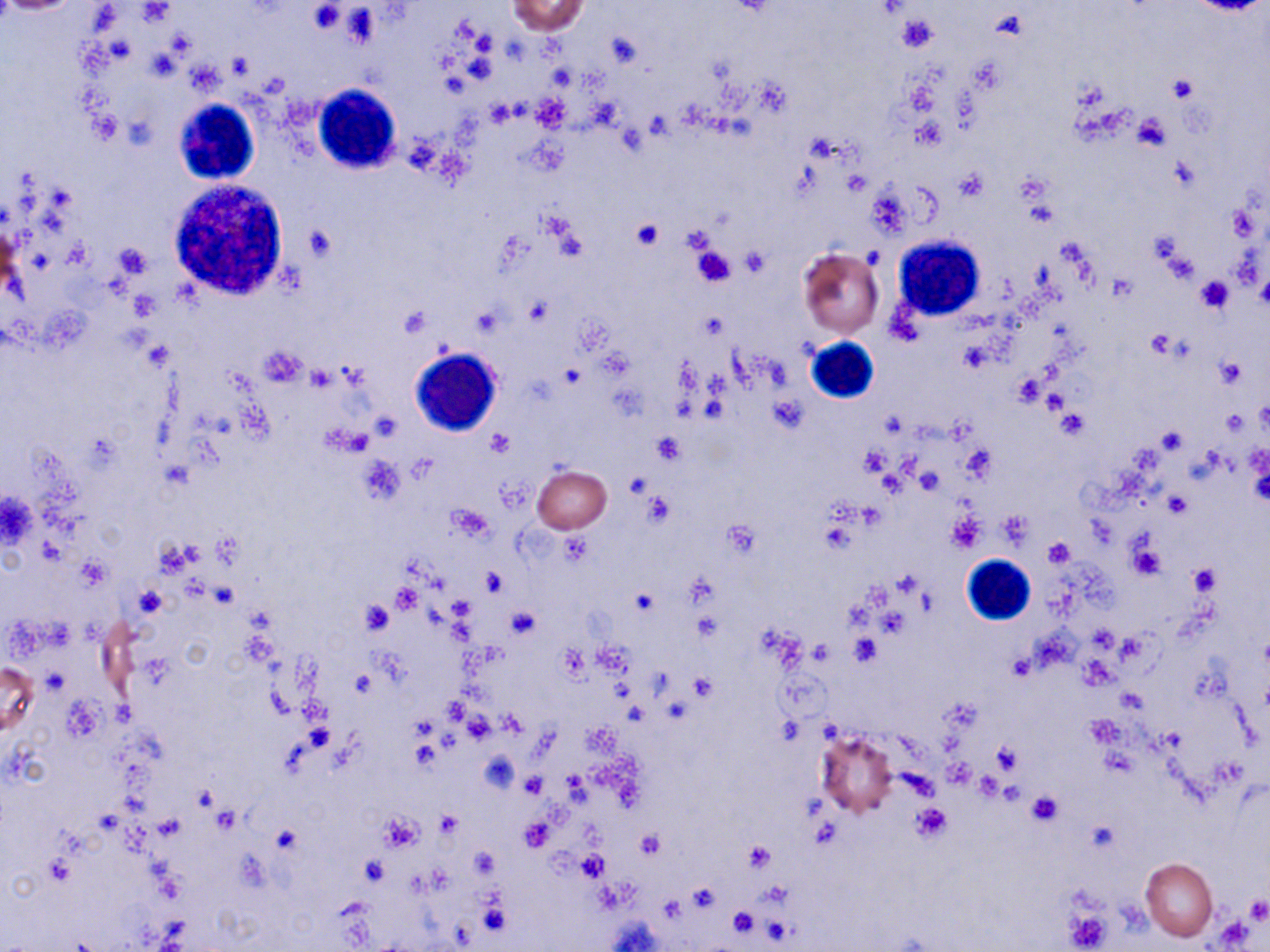
slide_level_diagnosis: no evidence of blood parasites
preparation: thin blood smear
white_blood_cell_locations: 'approximate bounding boxes as named x1/y1/x2/y2 corners in pixels: (x1=313, y1=85, x2=402, y2=175), (x1=172, y1=98, x2=260, y2=185), (x1=168, y1=177, x2=291, y2=301), (x1=893, y1=236, x2=983, y2=320), (x1=803, y1=337, x2=879, y2=404), (x1=410, y1=348, x2=501, y2=437), (x1=959, y1=554, x2=1036, y2=626)'
stain: May-Grünwald-Giemsa
modality: optical microscopy
image_size: 1270×952 pixels
magnification: 1000x
platelet_locations: 'approximate bounding boxes as named x1/y1/x2/y2 corners in pixels: (x1=309, y1=3, x2=344, y2=34), (x1=897, y1=14, x2=939, y2=53), (x1=606, y1=33, x2=640, y2=69), (x1=971, y1=58, x2=1006, y2=93), (x1=1169, y1=76, x2=1198, y2=102), (x1=1131, y1=115, x2=1170, y2=153), (x1=955, y1=170, x2=988, y2=203), (x1=630, y1=219, x2=664, y2=250), (x1=306, y1=225, x2=338, y2=261), (x1=112, y1=242, x2=153, y2=279), (x1=690, y1=246, x2=736, y2=289), (x1=740, y1=250, x2=771, y2=276), (x1=1195, y1=276, x2=1233, y2=314), (x1=1147, y1=331, x2=1177, y2=359), (x1=1216, y1=358, x2=1247, y2=388), (x1=307, y1=364, x2=337, y2=391), (x1=1056, y1=410, x2=1088, y2=440), (x1=1157, y1=428, x2=1185, y2=453), (x1=485, y1=429, x2=513, y2=457), (x1=652, y1=432, x2=686, y2=463), (x1=860, y1=447, x2=890, y2=478), (x1=1164, y1=492, x2=1190, y2=518), (x1=644, y1=494, x2=675, y2=526), (x1=448, y1=505, x2=492, y2=541), (x1=999, y1=511, x2=1033, y2=545), (x1=946, y1=514, x2=986, y2=552), (x1=560, y1=535, x2=591, y2=566), (x1=1045, y1=537, x2=1076, y2=567), (x1=1129, y1=542, x2=1166, y2=580), (x1=1188, y1=564, x2=1220, y2=595), (x1=481, y1=569, x2=508, y2=597), (x1=391, y1=583, x2=421, y2=614), (x1=632, y1=589, x2=658, y2=617), (x1=360, y1=600, x2=394, y2=636), (x1=506, y1=606, x2=540, y2=638), (x1=849, y1=635, x2=880, y2=667), (x1=1006, y1=654, x2=1034, y2=681), (x1=1080, y1=658, x2=1117, y2=690), (x1=689, y1=673, x2=716, y2=701), (x1=1084, y1=716, x2=1121, y2=748), (x1=991, y1=741, x2=1021, y2=775), (x1=522, y1=773, x2=548, y2=796), (x1=975, y1=775, x2=1004, y2=801), (x1=1026, y1=791, x2=1063, y2=826), (x1=911, y1=804, x2=952, y2=840), (x1=435, y1=811, x2=460, y2=840), (x1=380, y1=812, x2=423, y2=852), (x1=521, y1=818, x2=555, y2=851), (x1=637, y1=829, x2=666, y2=858), (x1=744, y1=841, x2=774, y2=871), (x1=578, y1=854, x2=606, y2=881), (x1=362, y1=855, x2=388, y2=885), (x1=46, y1=856, x2=74, y2=885), (x1=688, y1=885, x2=718, y2=913), (x1=658, y1=895, x2=683, y2=924), (x1=1244, y1=896, x2=1269, y2=923), (x1=727, y1=906, x2=758, y2=939), (x1=1065, y1=908, x2=1112, y2=950), (x1=761, y1=916, x2=795, y2=945)'
field_of_view: single
uninfected_red_blood_cell_locations: 'approximate bounding boxes as named x1/y1/x2/y2 corners in pixels: (x1=507, y1=0, x2=589, y2=35), (x1=797, y1=247, x2=885, y2=338), (x1=532, y1=466, x2=611, y2=534), (x1=0, y1=661, x2=40, y2=740), (x1=815, y1=730, x2=896, y2=817), (x1=1141, y1=858, x2=1218, y2=940)'